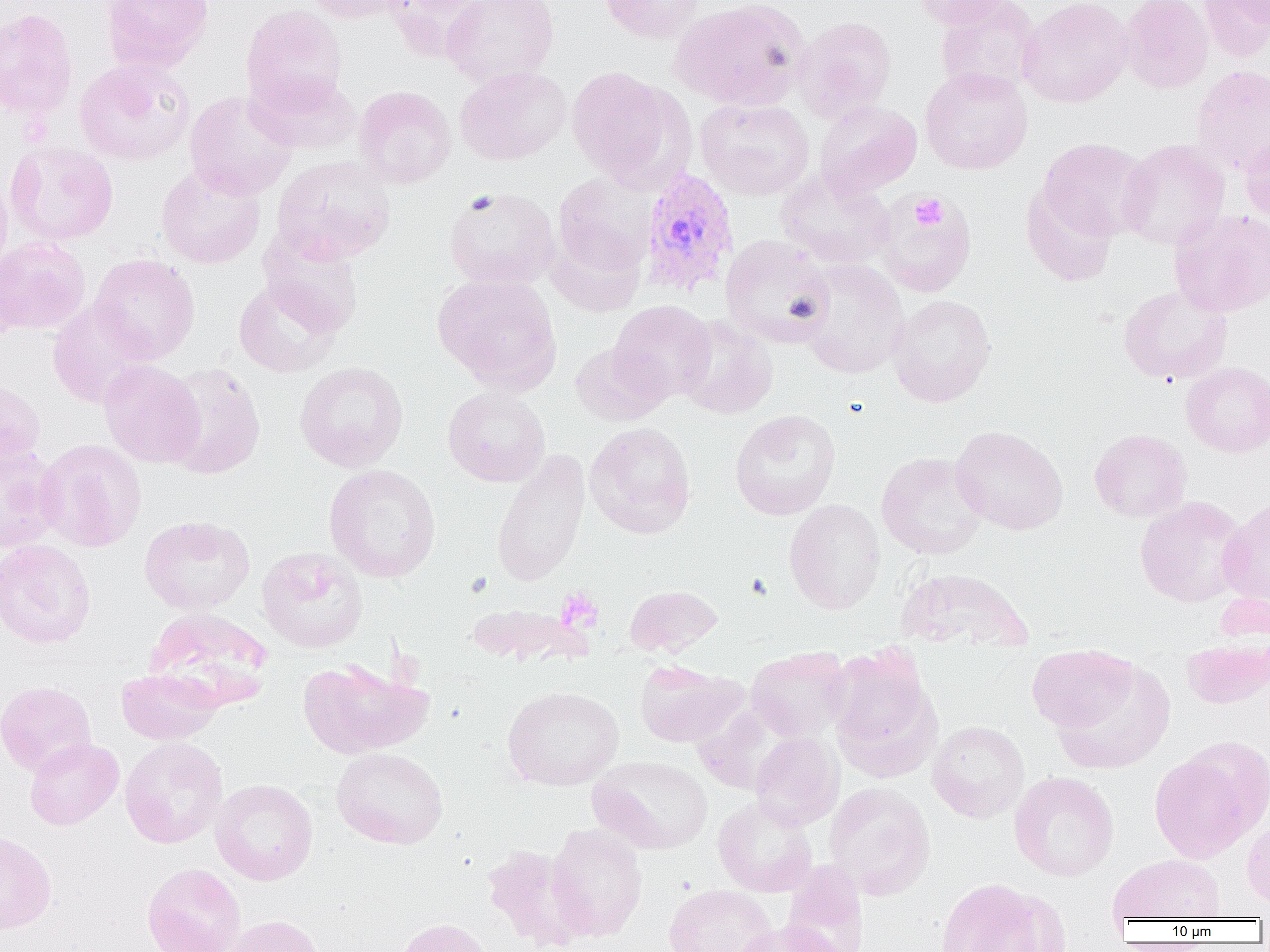

slide-level diagnosis = Plasmodium vivax
image size = 1270×952 pixels
magnification = 1000x
field of view = single
platelet locations = approximate bounding boxes as [x1, y1, x2, y2] in pixels: [911, 194, 947, 231], [556, 587, 603, 632]
modality = optical microscopy
Plasmodium vivax-infected red blood cell locations = approximate bounding boxes as [x1, y1, x2, y2] in pixels: [639, 166, 740, 298]
uninfected red blood cell locations = approximate bounding boxes as [x1, y1, x2, y2] in pixels: [101, 0, 213, 72], [302, 0, 408, 24], [381, 0, 487, 60], [442, 0, 559, 87], [599, 0, 704, 44], [669, 0, 811, 110], [910, 0, 1014, 29], [935, 0, 1042, 99], [1018, 0, 1134, 107], [1120, 0, 1213, 94], [1199, 0, 1269, 62], [1225, 0, 1270, 29], [240, 5, 347, 113], [0, 8, 78, 120], [794, 16, 898, 122], [74, 58, 195, 165], [455, 65, 572, 165], [1191, 65, 1270, 176], [566, 66, 681, 186], [920, 67, 1032, 174], [246, 71, 362, 155], [353, 85, 456, 189], [184, 91, 297, 200], [695, 98, 815, 200], [814, 101, 922, 198], [1240, 132, 1270, 224], [1038, 137, 1152, 240], [1118, 138, 1229, 250], [5, 141, 119, 245], [271, 155, 397, 264], [156, 163, 266, 268], [776, 167, 896, 269], [0, 169, 12, 280], [553, 172, 657, 276], [1021, 184, 1117, 286], [443, 187, 560, 290], [875, 192, 976, 296], [1169, 209, 1270, 317], [258, 227, 364, 337], [548, 229, 648, 317], [720, 235, 835, 348], [0, 237, 91, 335], [89, 254, 200, 364], [798, 259, 909, 379], [432, 273, 562, 392], [232, 278, 344, 377], [1118, 284, 1233, 385], [888, 294, 997, 407], [47, 300, 154, 408], [609, 300, 716, 404], [675, 315, 778, 419], [569, 342, 670, 426], [99, 359, 205, 468], [294, 361, 408, 472], [1181, 362, 1270, 457], [162, 363, 266, 480], [0, 378, 45, 472], [442, 386, 550, 486], [730, 409, 841, 520], [585, 422, 696, 538], [950, 425, 1068, 535], [1089, 429, 1191, 522], [35, 438, 147, 552], [0, 445, 63, 552], [490, 448, 591, 587], [876, 452, 988, 560], [323, 464, 441, 582], [1135, 496, 1247, 607], [1217, 496, 1270, 609], [784, 499, 885, 615], [139, 515, 255, 615], [0, 539, 97, 649], [257, 547, 368, 653], [897, 567, 1033, 653], [623, 584, 723, 657], [466, 603, 592, 666], [144, 607, 274, 711], [1182, 635, 1270, 709], [1026, 644, 1137, 733], [746, 646, 852, 741], [828, 651, 941, 780], [298, 657, 431, 759], [634, 659, 745, 747], [1054, 660, 1175, 774], [116, 668, 223, 744], [0, 680, 97, 776], [502, 685, 623, 790], [694, 702, 795, 795], [927, 720, 1030, 823], [750, 732, 843, 830], [119, 736, 228, 849], [25, 738, 124, 830], [332, 747, 448, 849], [1150, 750, 1261, 862], [588, 755, 713, 854], [1009, 771, 1119, 881], [210, 778, 318, 885], [824, 782, 935, 898], [713, 795, 818, 897], [1242, 818, 1270, 911], [546, 823, 647, 941], [0, 829, 57, 935], [482, 844, 590, 951], [1108, 854, 1225, 923], [781, 861, 868, 952], [142, 863, 246, 952], [935, 878, 1056, 952], [664, 884, 777, 952], [222, 915, 325, 952], [393, 917, 494, 952], [732, 920, 844, 952]
preparation = thin blood film